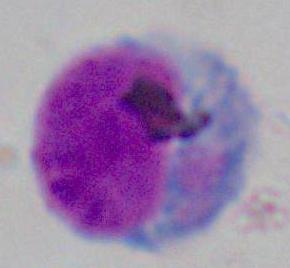

Photomicrograph. A leukocyte is seen. Captured at 1000x magnification.